Give the extent of all uninfected red blood cells.
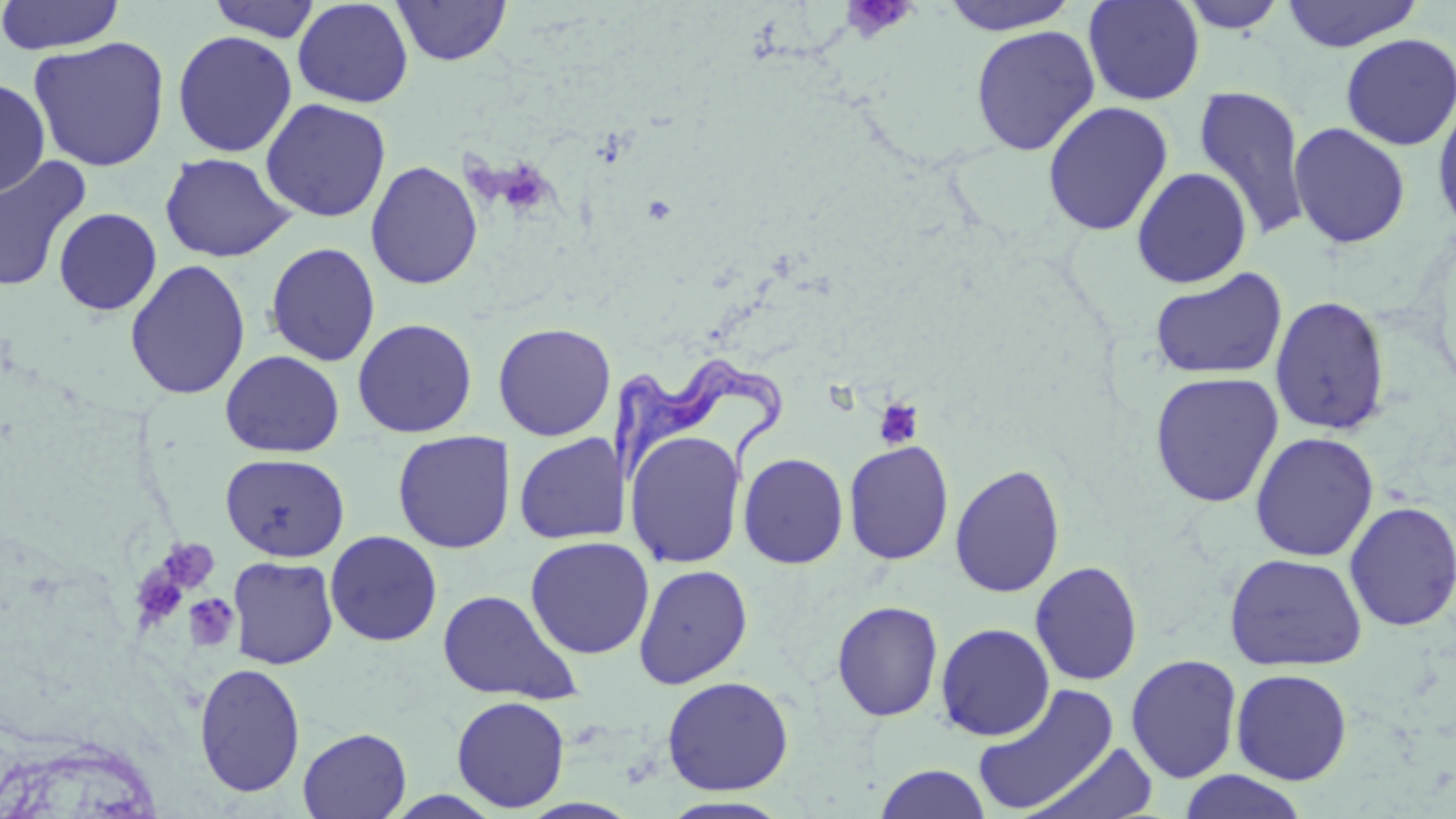
Approximate bounding boxes as (x1,y1)-(x2,y2) corner pairs in pixels.
Uninfected red blood cells: (0,0)-(126,55), (208,0)-(322,42), (1082,0)-(1205,105), (1280,0)-(1423,52), (293,1)-(413,108), (393,1)-(511,66), (939,1)-(1080,35), (1177,1)-(1289,33), (970,25)-(1099,156), (172,30)-(297,158), (1340,33)-(1456,151), (28,35)-(171,172), (0,79)-(51,198), (1193,84)-(1312,242), (260,98)-(391,223), (1432,99)-(1456,236), (1042,101)-(1174,237), (1288,122)-(1411,249), (160,152)-(295,263), (0,156)-(93,293), (365,160)-(483,290), (1132,167)-(1252,288), (53,207)-(162,315), (264,242)-(381,367), (124,260)-(251,401), (1149,267)-(1288,381), (1269,295)-(1392,436), (352,318)-(477,438), (493,322)-(616,441), (220,350)-(345,457), (1149,372)-(1285,508), (393,430)-(514,553), (625,430)-(745,568), (1249,432)-(1379,561), (513,433)-(628,544), (842,439)-(955,565), (738,451)-(849,569), (221,452)-(349,562), (949,463)-(1066,599), (1343,501)-(1456,632), (325,530)-(443,647), (525,536)-(655,659), (1224,552)-(1367,672), (227,556)-(339,669), (1029,560)-(1143,686), (633,563)-(754,689), (436,589)-(581,704), (830,599)-(944,722), (935,622)-(1055,741), (1125,653)-(1243,783), (193,662)-(306,798), (1231,668)-(1352,785), (662,676)-(794,795), (971,683)-(1121,816), (451,695)-(570,813), (298,727)-(411,819), (1026,742)-(1160,817), (874,764)-(992,819), (1178,770)-(1308,818), (658,796)-(794,818).

Summary:
  - Platelet locations: (858,0)-(909,30), (505,173)-(547,214), (874,399)-(925,450), (154,539)-(220,597), (131,561)-(191,632), (183,594)-(240,652)
  - Trypanosoma brucei locations: (599,358)-(791,479)
  - Slide-level diagnosis: Trypanosoma brucei
  - Field of view: one of a larger specimen
  - Modality: optical microscopy
  - Preparation: thin blood film
  - Image size: 1456×819 pixels
  - Magnification: 1000x
  - Stain: May-Grünwald-Giemsa